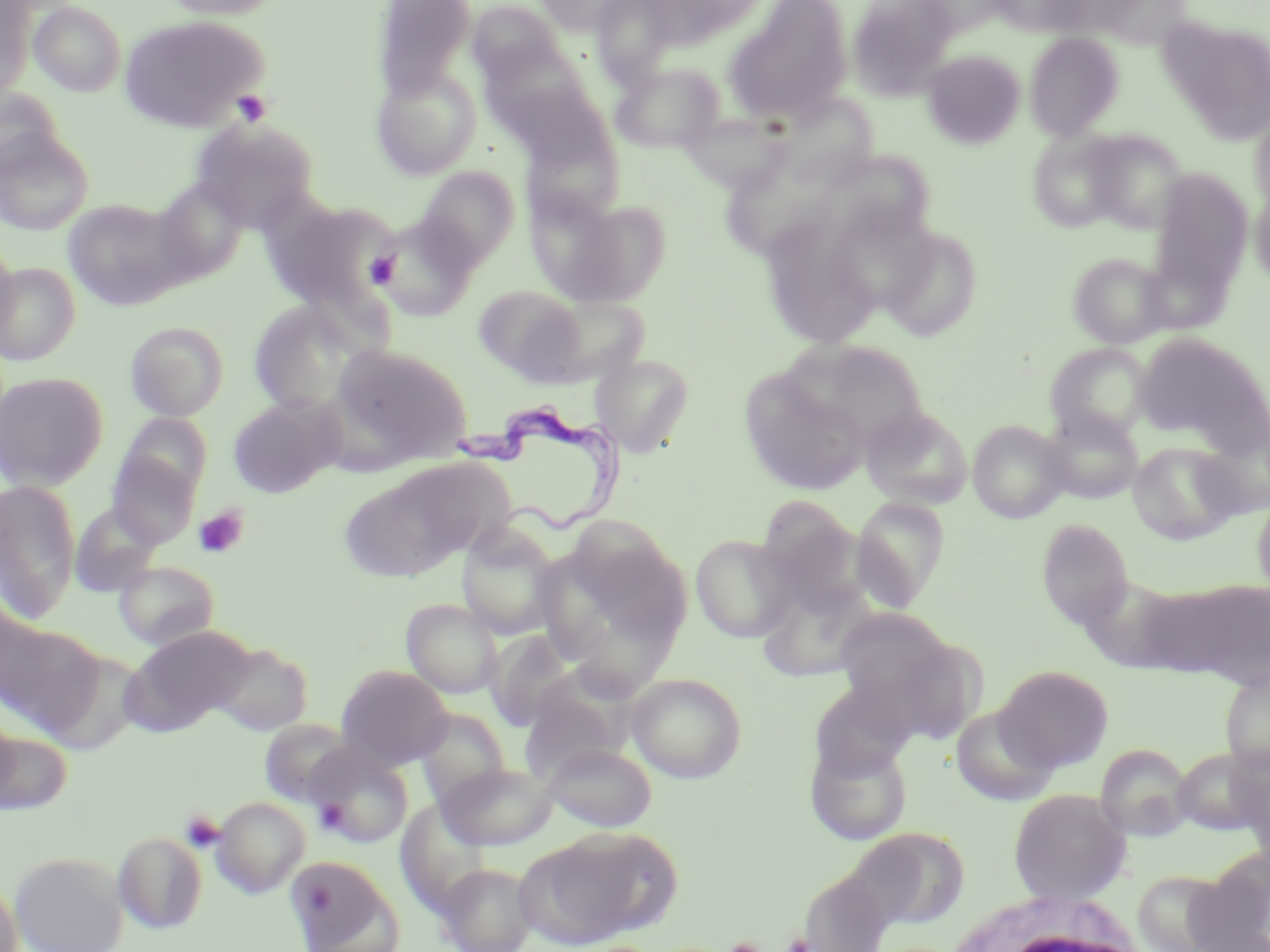
Summary:
  - Coordinate format: approximate bounding boxes as named x1/y1/x2/y2 corners in pixels
  - Platelet locations: (x1=233, y1=90, x2=272, y2=126), (x1=366, y1=252, x2=400, y2=287), (x1=193, y1=506, x2=249, y2=558), (x1=315, y1=801, x2=349, y2=834), (x1=181, y1=811, x2=225, y2=853), (x1=784, y1=934, x2=813, y2=952), (x1=725, y1=937, x2=764, y2=952)
  - White blood cell locations: (x1=944, y1=890, x2=1153, y2=952)
  - Trypanosoma brucei locations: (x1=446, y1=396, x2=633, y2=537)
  - Uninfected red blood cell locations: (x1=159, y1=0, x2=289, y2=20), (x1=374, y1=0, x2=477, y2=100), (x1=533, y1=0, x2=647, y2=35), (x1=846, y1=0, x2=959, y2=101), (x1=991, y1=0, x2=1096, y2=36), (x1=1028, y1=0, x2=1158, y2=41), (x1=29, y1=1, x2=126, y2=97), (x1=721, y1=1, x2=853, y2=127), (x1=466, y1=2, x2=568, y2=87), (x1=0, y1=3, x2=35, y2=102), (x1=119, y1=15, x2=270, y2=133), (x1=1159, y1=18, x2=1270, y2=144), (x1=1024, y1=32, x2=1125, y2=141), (x1=477, y1=40, x2=598, y2=139), (x1=921, y1=50, x2=1025, y2=149), (x1=611, y1=61, x2=725, y2=153), (x1=371, y1=64, x2=481, y2=179), (x1=493, y1=72, x2=613, y2=165), (x1=0, y1=87, x2=65, y2=180), (x1=775, y1=97, x2=879, y2=189), (x1=680, y1=107, x2=810, y2=197), (x1=1248, y1=108, x2=1270, y2=213), (x1=190, y1=118, x2=320, y2=232), (x1=518, y1=121, x2=624, y2=227), (x1=1080, y1=128, x2=1191, y2=233), (x1=1026, y1=129, x2=1132, y2=233), (x1=0, y1=130, x2=94, y2=236), (x1=839, y1=161, x2=936, y2=236), (x1=715, y1=166, x2=839, y2=258), (x1=414, y1=167, x2=519, y2=270), (x1=1148, y1=169, x2=1254, y2=293), (x1=151, y1=180, x2=248, y2=285), (x1=1250, y1=184, x2=1270, y2=290), (x1=534, y1=189, x2=670, y2=307), (x1=63, y1=198, x2=186, y2=310), (x1=263, y1=198, x2=401, y2=313), (x1=821, y1=199, x2=938, y2=317), (x1=368, y1=217, x2=478, y2=319), (x1=877, y1=225, x2=985, y2=342), (x1=0, y1=239, x2=17, y2=352), (x1=1067, y1=251, x2=1172, y2=349), (x1=773, y1=259, x2=875, y2=345), (x1=0, y1=262, x2=80, y2=366), (x1=473, y1=285, x2=589, y2=384), (x1=528, y1=293, x2=651, y2=387), (x1=248, y1=300, x2=369, y2=415), (x1=125, y1=321, x2=229, y2=421), (x1=1133, y1=331, x2=1268, y2=451), (x1=787, y1=336, x2=935, y2=442), (x1=330, y1=343, x2=471, y2=464), (x1=1045, y1=343, x2=1155, y2=441), (x1=590, y1=352, x2=695, y2=458), (x1=738, y1=366, x2=874, y2=497), (x1=0, y1=372, x2=108, y2=491), (x1=228, y1=396, x2=344, y2=498), (x1=858, y1=407, x2=974, y2=511), (x1=1039, y1=409, x2=1144, y2=504), (x1=117, y1=412, x2=213, y2=501), (x1=1197, y1=417, x2=1270, y2=519), (x1=967, y1=419, x2=1072, y2=523), (x1=1129, y1=441, x2=1242, y2=544), (x1=106, y1=449, x2=200, y2=547), (x1=353, y1=457, x2=508, y2=578), (x1=0, y1=479, x2=82, y2=622), (x1=1251, y1=491, x2=1270, y2=600), (x1=850, y1=496, x2=950, y2=610), (x1=70, y1=501, x2=165, y2=597), (x1=1037, y1=519, x2=1134, y2=633), (x1=456, y1=524, x2=563, y2=640), (x1=555, y1=527, x2=692, y2=667), (x1=691, y1=534, x2=797, y2=642), (x1=113, y1=560, x2=219, y2=650), (x1=1080, y1=576, x2=1191, y2=679), (x1=1160, y1=577, x2=1270, y2=689), (x1=755, y1=578, x2=877, y2=682), (x1=401, y1=599, x2=503, y2=699), (x1=832, y1=608, x2=961, y2=705), (x1=0, y1=619, x2=102, y2=732), (x1=122, y1=626, x2=254, y2=733), (x1=486, y1=630, x2=577, y2=731), (x1=819, y1=635, x2=959, y2=751), (x1=212, y1=642, x2=313, y2=736), (x1=995, y1=664, x2=1114, y2=772), (x1=336, y1=665, x2=453, y2=769), (x1=1220, y1=670, x2=1270, y2=776), (x1=626, y1=672, x2=747, y2=783), (x1=520, y1=681, x2=626, y2=783), (x1=809, y1=682, x2=915, y2=781), (x1=950, y1=704, x2=1060, y2=807), (x1=413, y1=707, x2=511, y2=803), (x1=0, y1=709, x2=20, y2=813), (x1=258, y1=719, x2=357, y2=807), (x1=1, y1=730, x2=73, y2=815), (x1=805, y1=738, x2=913, y2=846), (x1=307, y1=741, x2=413, y2=848), (x1=543, y1=742, x2=657, y2=832), (x1=1095, y1=743, x2=1193, y2=842), (x1=1173, y1=747, x2=1266, y2=834), (x1=437, y1=762, x2=557, y2=850), (x1=1008, y1=788, x2=1132, y2=904), (x1=211, y1=796, x2=311, y2=898), (x1=405, y1=797, x2=495, y2=920), (x1=854, y1=826, x2=970, y2=929), (x1=514, y1=829, x2=661, y2=948), (x1=113, y1=831, x2=208, y2=934), (x1=8, y1=851, x2=130, y2=952), (x1=286, y1=855, x2=404, y2=951), (x1=1188, y1=855, x2=1270, y2=951), (x1=437, y1=862, x2=538, y2=952), (x1=798, y1=868, x2=894, y2=952), (x1=0, y1=872, x2=24, y2=952)
  - Slide-level diagnosis: Trypanosoma brucei
  - Modality: optical microscopy
  - Stain: May-Grünwald-Giemsa
  - Preparation: thin blood smear
  - Field of view: one of a larger specimen
  - Image size: 1270×952 pixels
  - Magnification: 1000x